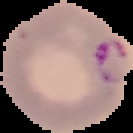

{
  "image_size": "133×133 pixels",
  "malaria_status": "parasitized",
  "preparation": "thin blood film",
  "image_type": "segmented cell region with the area outside set to black"
}